Locate and identify every blood parasite.
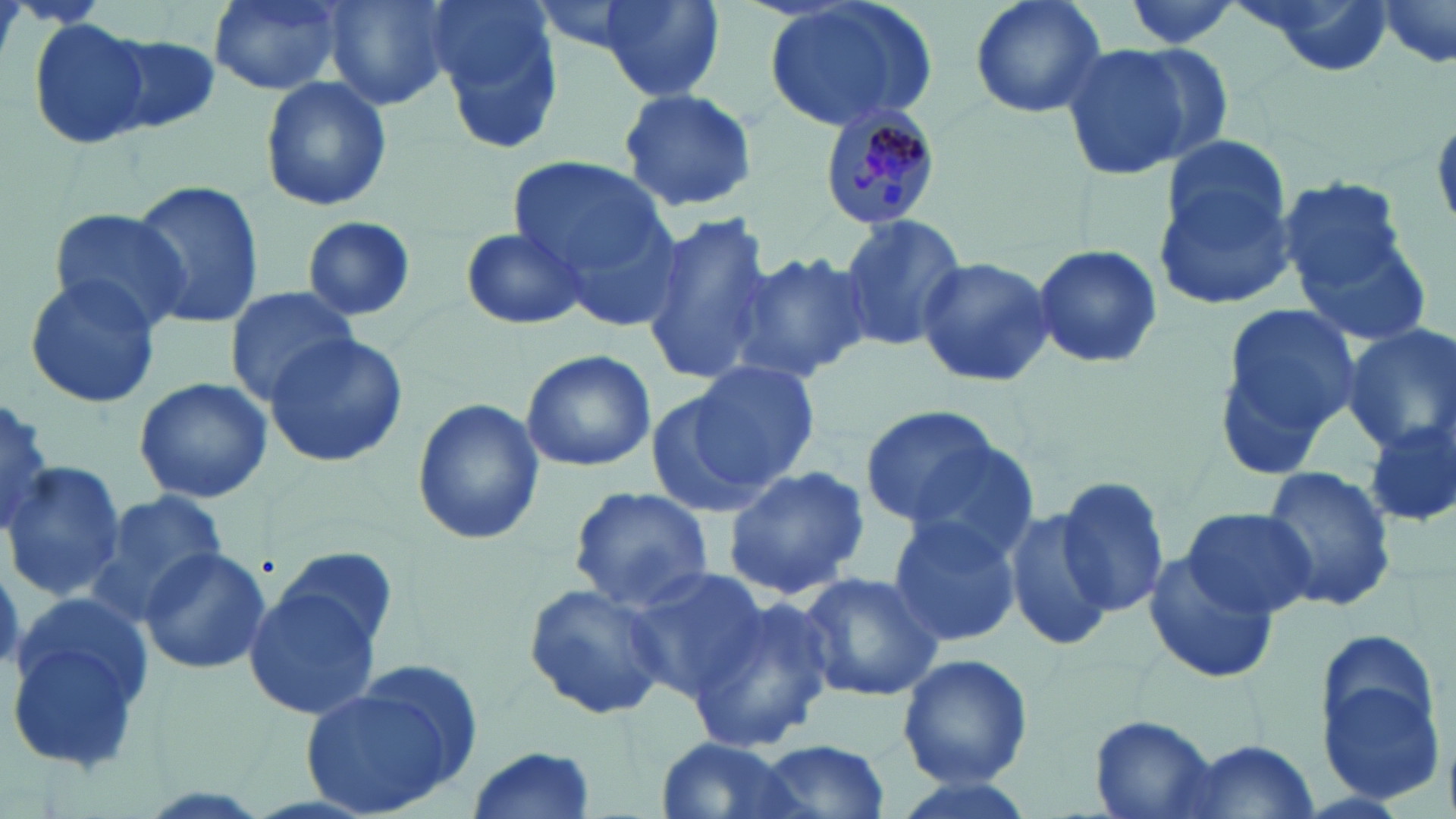

Approximate bounding boxes as [x1, y1, x2, y2] in pixels.
Plasmodium malariae-infected red blood cells: [820, 106, 941, 230].
No Plasmodium falciparum, Plasmodium ovale, Plasmodium vivax, Babesia divergens, or Trypanosoma brucei observed.

Uninfected red blood cell locations: [209, 0, 347, 95], [324, 0, 455, 111], [596, 0, 724, 101], [762, 0, 941, 133], [969, 0, 1108, 120], [1116, 0, 1248, 52], [1231, 0, 1400, 79], [1377, 1, 1453, 67], [427, 2, 569, 155], [30, 20, 150, 146], [103, 35, 221, 135], [1058, 42, 1191, 180], [1110, 43, 1235, 169], [259, 76, 391, 212], [617, 87, 760, 212], [1163, 136, 1289, 251], [507, 154, 670, 290], [1153, 166, 1301, 308], [1278, 176, 1412, 302], [131, 180, 264, 330], [48, 208, 189, 330], [640, 210, 774, 388], [836, 212, 967, 349], [297, 218, 419, 323], [460, 225, 589, 331], [1299, 227, 1435, 347], [1030, 242, 1164, 369], [731, 248, 875, 383], [914, 255, 1056, 389], [23, 274, 160, 411], [225, 287, 360, 402], [1211, 301, 1364, 472], [1341, 325, 1456, 457], [262, 333, 407, 468], [519, 348, 657, 471], [689, 360, 823, 488], [134, 378, 271, 503], [644, 382, 781, 520], [2, 397, 53, 537], [410, 398, 546, 548], [860, 404, 1005, 528], [1365, 418, 1455, 528], [896, 435, 1042, 562], [4, 462, 123, 600], [720, 462, 871, 600], [1261, 466, 1398, 615], [1055, 475, 1172, 619], [567, 487, 715, 611], [87, 492, 229, 622], [1180, 505, 1318, 621], [1004, 507, 1114, 653], [885, 514, 1022, 648], [138, 547, 271, 675], [275, 549, 399, 655], [1143, 549, 1281, 686], [622, 565, 772, 698], [799, 570, 944, 702], [242, 582, 383, 722], [522, 582, 673, 723], [686, 595, 837, 755], [6, 599, 154, 776], [1316, 644, 1450, 806], [898, 651, 1033, 789], [301, 675, 473, 819], [1090, 715, 1218, 818], [651, 737, 814, 819], [756, 738, 893, 818], [1167, 740, 1325, 817], [463, 745, 597, 818], [886, 772, 1040, 819]. Slide-level diagnosis: Plasmodium malariae. Thin blood film. Image is 1456×819 pixels. Light microscopy. Captured at 1000x magnification. May-Grünwald-Giemsa-stained preparation. One field of a larger specimen.